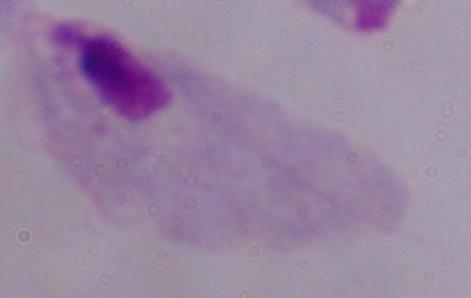 Photomicrograph. A trichomonad is seen. 1000x magnification.